Locate every Plasmodium parasite.
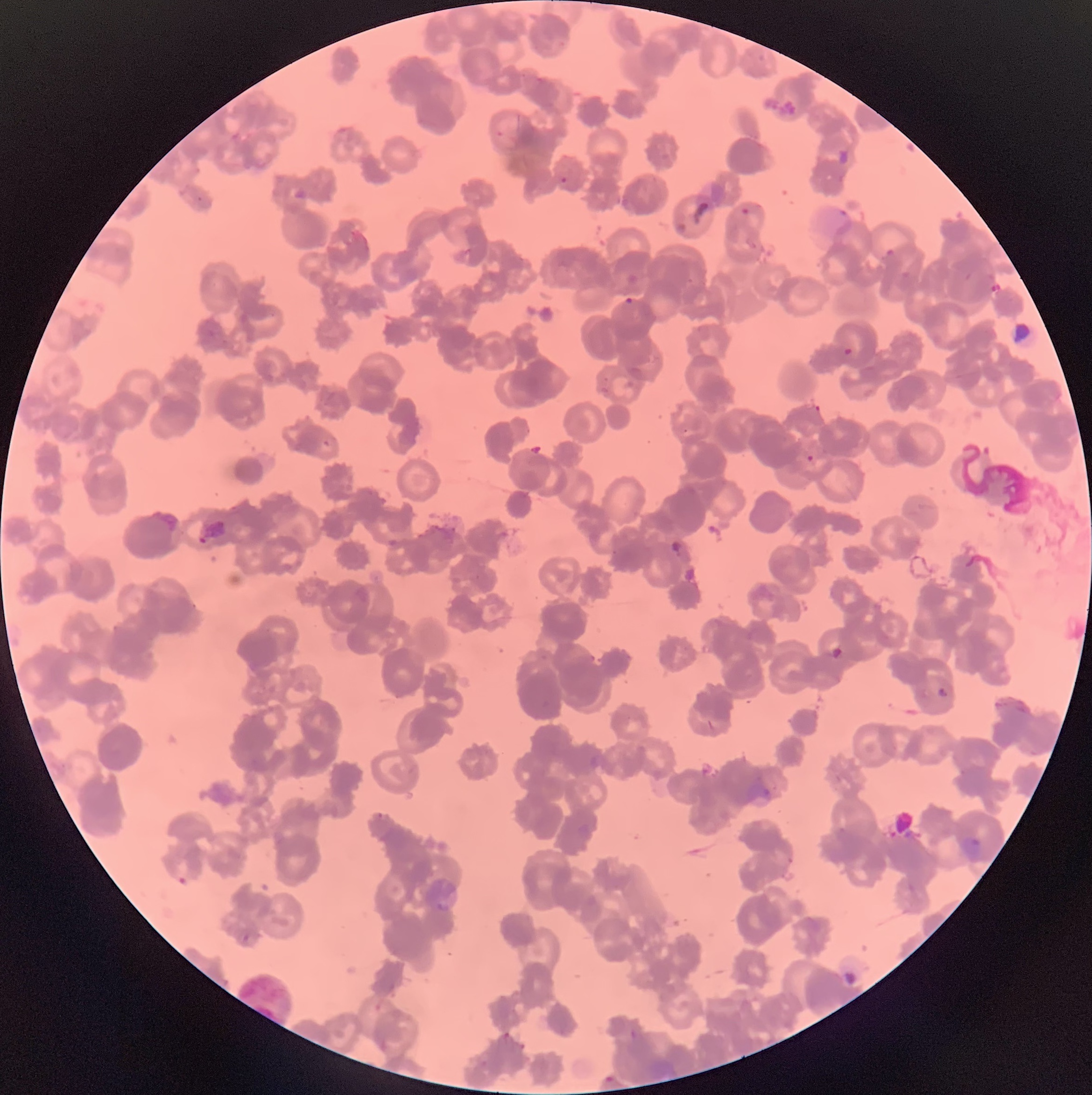

Approximate bounding boxes as [x1, y1, x2, y2] in pixels.
Plasmodium parasites: [559, 173, 570, 184], [737, 205, 754, 217], [805, 454, 815, 462], [589, 654, 595, 662], [936, 687, 948, 697], [376, 812, 387, 819], [959, 835, 981, 855], [175, 870, 192, 888], [627, 1027, 638, 1040], [501, 1031, 513, 1042], [517, 1040, 528, 1051], [478, 1057, 491, 1070], [603, 1072, 619, 1084].

Summary:
  - Red blood cell morphology: rouleaux formation
  - Image size: 1092×1095 pixels
  - Modality: light microscopy
  - Preparation: thin blood film